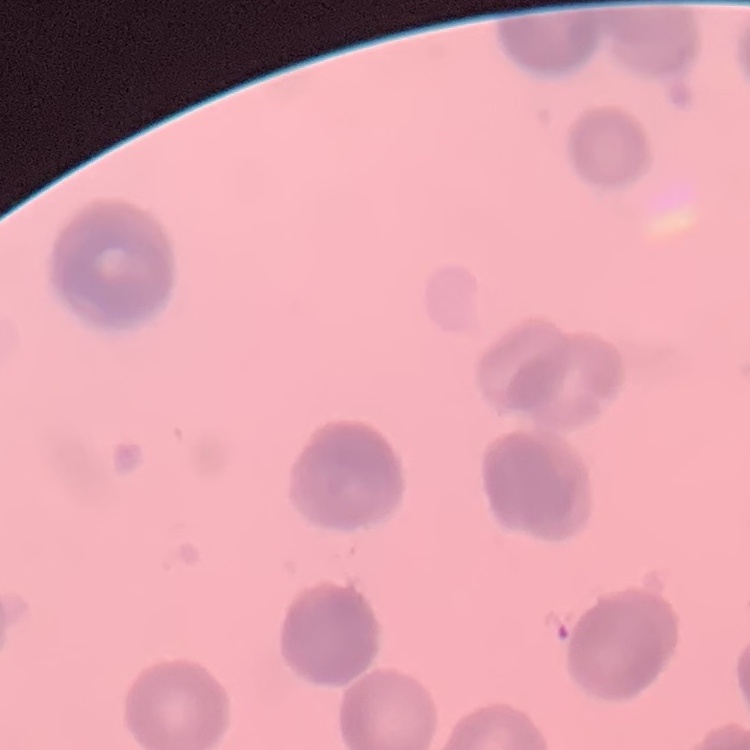

red blood cell morphology = rouleaux formation
stain = Field's or Giemsa
image type = square crop of a larger photomicrograph
preparation = thin blood smear